Locate every malaria parasite and every leukocyte.
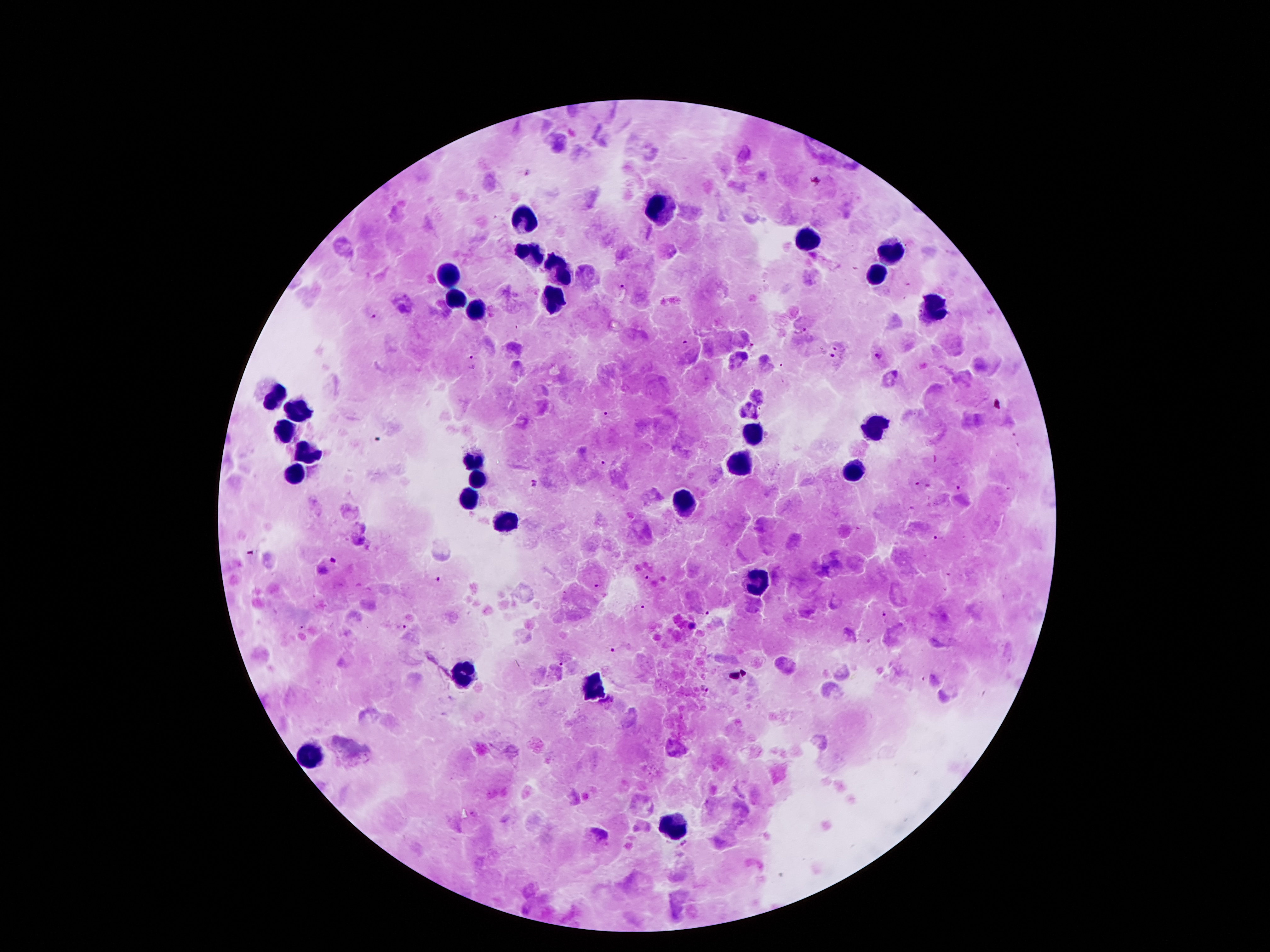
Approximate object centers, in pixels from the top-left corner.
Malaria parasites: (x=528, y=171), (x=622, y=286), (x=374, y=316), (x=801, y=331), (x=685, y=342), (x=836, y=347), (x=832, y=354), (x=877, y=356), (x=472, y=358), (x=606, y=415), (x=375, y=439), (x=604, y=463), (x=535, y=484), (x=917, y=484), (x=958, y=488), (x=935, y=537), (x=334, y=559), (x=648, y=578), (x=438, y=580), (x=599, y=586), (x=639, y=608), (x=706, y=614), (x=885, y=614), (x=401, y=627), (x=610, y=651), (x=561, y=664), (x=706, y=689).
Leukocytes: (x=663, y=208), (x=520, y=215), (x=808, y=238), (x=891, y=248), (x=529, y=253), (x=560, y=263), (x=874, y=273), (x=445, y=275), (x=555, y=293), (x=458, y=298), (x=933, y=310), (x=476, y=313), (x=271, y=397), (x=297, y=413), (x=871, y=427), (x=285, y=433), (x=755, y=438), (x=307, y=451), (x=473, y=463), (x=743, y=463), (x=849, y=473), (x=297, y=477), (x=479, y=478), (x=469, y=500), (x=684, y=503), (x=508, y=520), (x=758, y=585), (x=468, y=673), (x=593, y=688), (x=310, y=754), (x=671, y=830).

{
  "preparation": "thick blood film",
  "magnification": "100x",
  "patient_malaria_status": "positive for Plasmodium falciparum",
  "field_of_view": "single",
  "capture": "smartphone camera through the microscope eyepiece",
  "stain": "Giemsa",
  "image_size": "1270×952 pixels"
}